Describe the morphology of the erythrocytes.
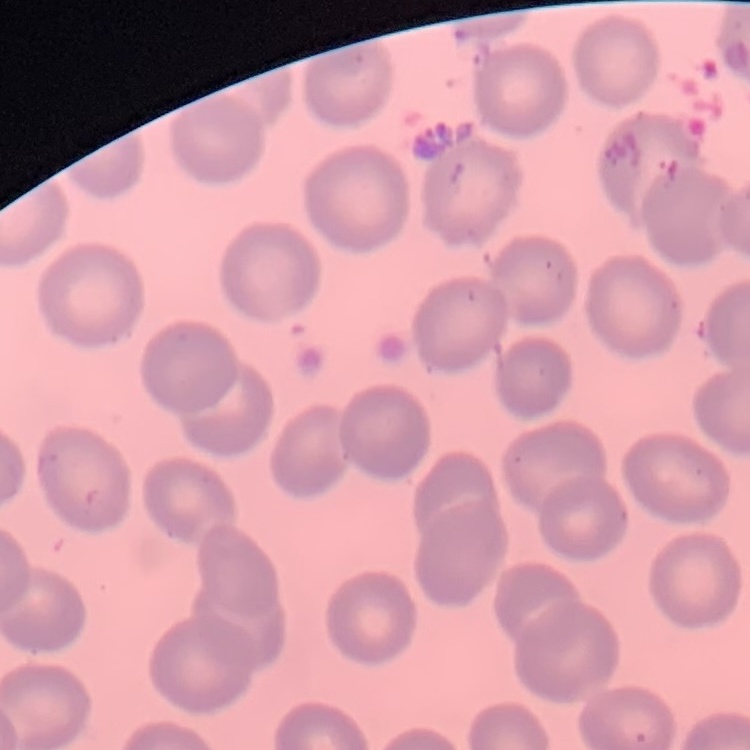

They show no rouleaux formation.

Thin peripheral smear. Square crop of a larger photomicrograph. Stained with either Field's or Giemsa.